Locate every blood parasite and identify its species.
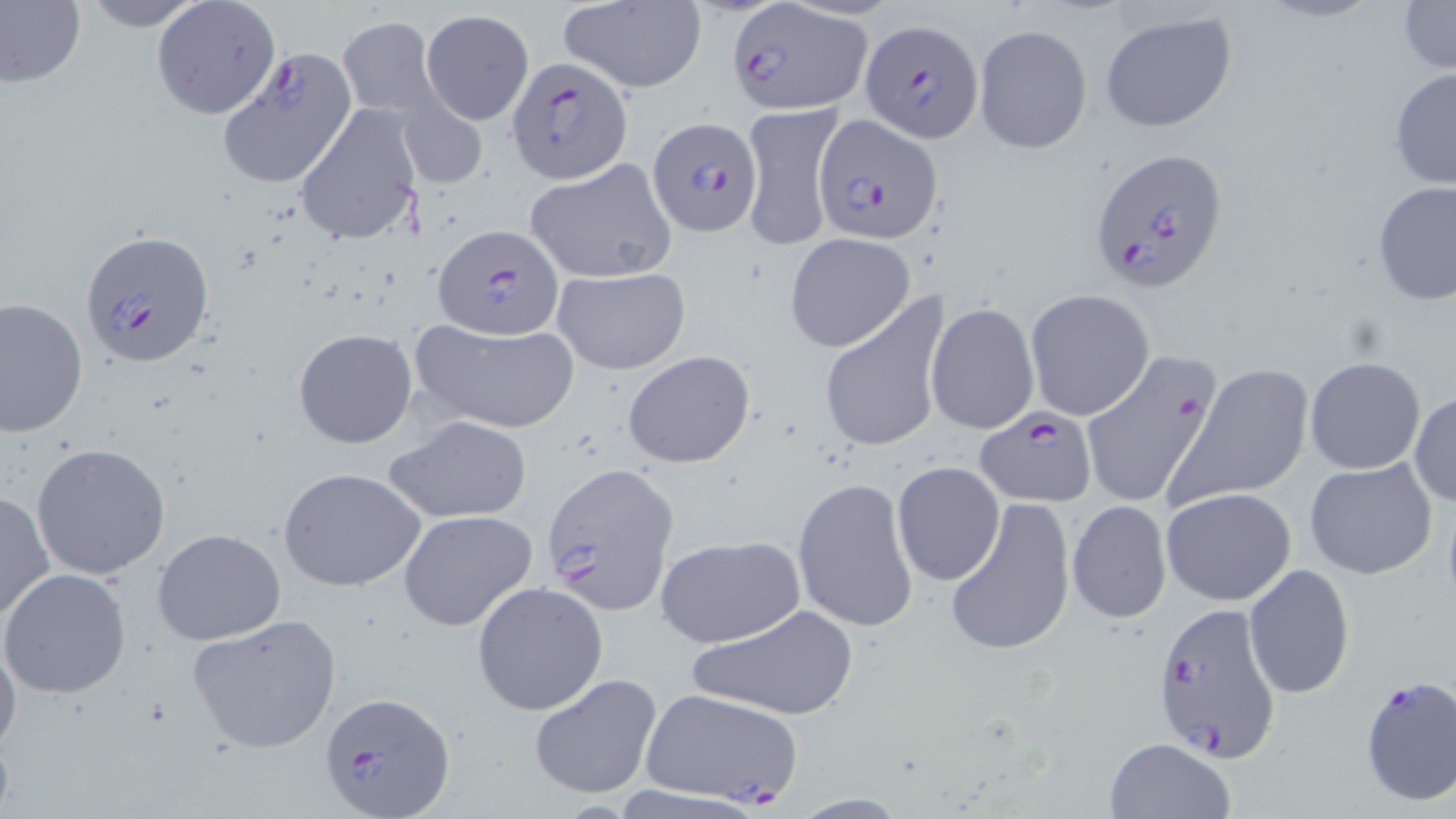

Approximate bounding boxes as (x1, y1, x2, y2) in pixels.
Plasmodium falciparum-infected red blood cells: (726, 0, 870, 114), (864, 18, 984, 141), (506, 57, 634, 183), (812, 113, 944, 241), (649, 116, 763, 237), (1086, 146, 1229, 293), (432, 221, 566, 340), (79, 227, 216, 370), (975, 409, 1097, 507), (539, 462, 680, 614), (1152, 600, 1283, 764), (1356, 676, 1455, 806), (320, 692, 451, 815).
No Plasmodium ovale, Plasmodium malariae, Plasmodium vivax, Babesia divergens, or Trypanosoma brucei observed.

slide-level diagnosis = Plasmodium falciparum
uninfected red blood cell locations = approximate bounding boxes as (x1, y1, x2, y2) in pixels: (0, 0, 85, 87), (77, 0, 208, 30), (150, 0, 283, 122), (557, 1, 707, 93), (1398, 1, 1456, 75), (421, 10, 534, 125), (1099, 10, 1238, 133), (337, 15, 445, 121), (973, 22, 1092, 154), (215, 48, 359, 191), (1389, 66, 1456, 190), (396, 92, 489, 193), (738, 101, 847, 252), (293, 102, 423, 246), (525, 160, 679, 285), (1372, 181, 1456, 305), (784, 232, 916, 352), (552, 267, 691, 375), (817, 289, 951, 457), (1025, 291, 1155, 421), (0, 298, 88, 437), (925, 303, 1039, 434), (410, 317, 581, 433), (293, 328, 418, 448), (621, 349, 755, 468), (1079, 349, 1220, 510), (1304, 356, 1427, 474), (1172, 362, 1314, 507), (1409, 392, 1455, 507), (383, 415, 533, 524), (31, 442, 172, 580), (1304, 457, 1438, 580), (893, 461, 1005, 586), (278, 466, 425, 593), (792, 476, 918, 633), (1161, 487, 1296, 606), (0, 489, 54, 626), (946, 498, 1074, 657), (1067, 500, 1172, 624), (397, 509, 538, 632), (153, 529, 286, 645), (651, 534, 807, 648), (1244, 563, 1354, 701), (0, 568, 131, 699), (471, 581, 608, 716), (685, 601, 860, 724), (187, 615, 342, 753), (0, 635, 22, 759), (527, 672, 664, 800), (642, 687, 805, 807), (1102, 736, 1236, 819)
magnification = 1000x
modality = optical microscopy
preparation = thin blood smear
stain = May-Grünwald-Giemsa
image size = 1456×819 pixels
field of view = one of a larger specimen